Point out leukocytes.
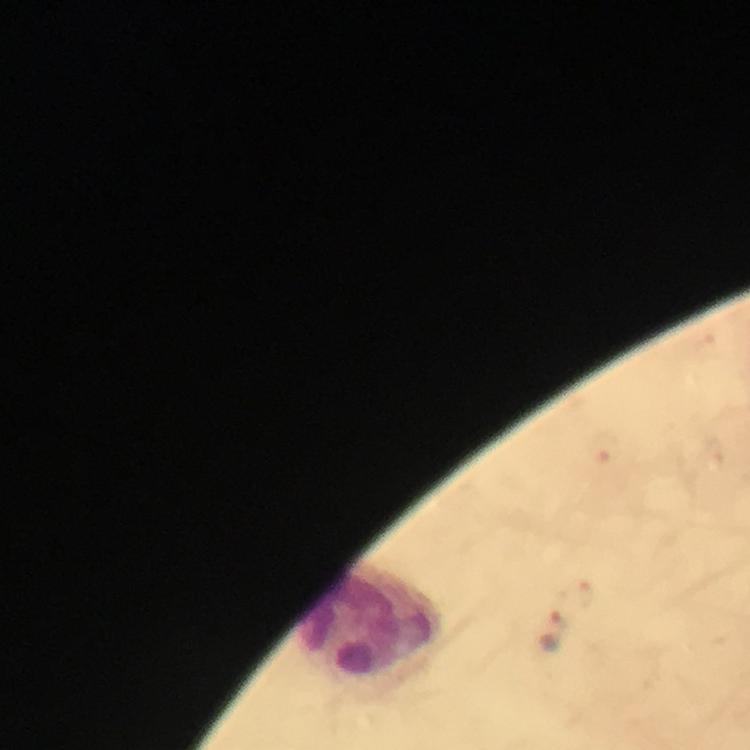
Approximate object centers, in pixels from the top-left corner.
Leukocytes: (x=372, y=620).

Plasmodium parasite locations: (x=604, y=450), (x=557, y=631). Thick smear. Cropped region of a single field of view. Photographed through the microscope with a smartphone camera. Image is 750×750 pixels. From a diagnostic examination for malaria. Immersion oil was used. At 100x magnification. Giemsa stain.